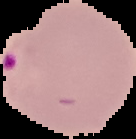
image size = 136×139 pixels
result = Plasmodium parasites detected
image type = cell region segmented out of the field of view; surrounding area masked to black
preparation = thin blood smear